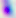

modality = micrograph
magnification = 400x
identification = Toxoplasma gondii